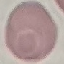

Summary:
  - Result: no malaria parasites seen
  - Preparation: thin blood smear
  - Capture: smartphone camera at the microscope eyepiece
  - Stain: Giemsa
  - Image type: cell patch, automatically extracted from a larger field of view and resized to 64 × 64 pixels